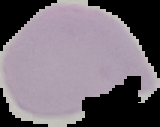 Malaria status: uninfected. Segmented cell region on a black background. From a thin blood film. Image is 160×127 pixels.